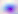

modality = photomicrograph
magnification = 400x
identification = Toxoplasma gondii